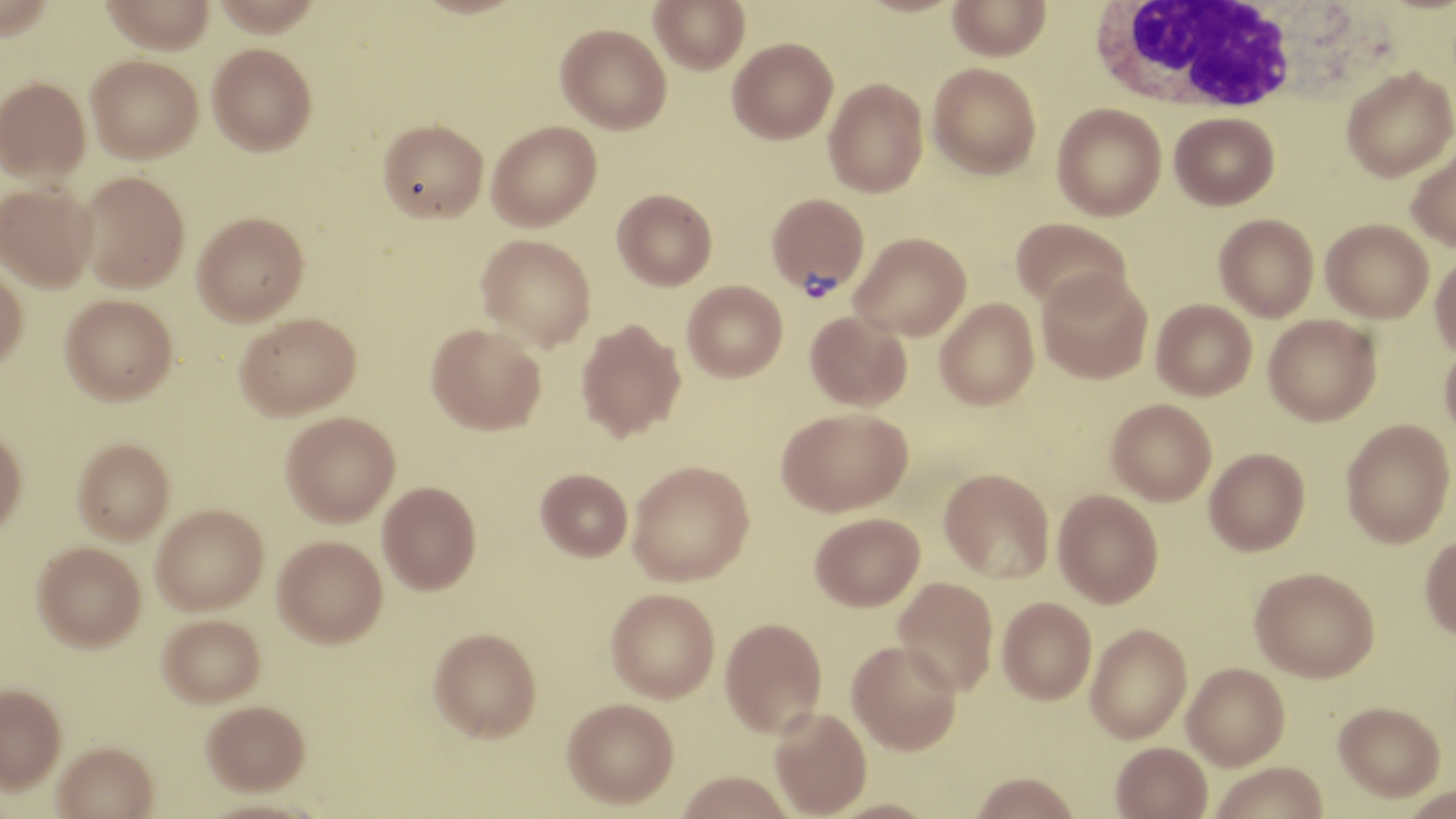

Approximate bounding boxes as named x1/y1/x2/y2 corners in pixels. Plasmodium vivax-infected red blood cell locations: (x1=767, y1=193, x2=869, y2=298). Uninfected red blood cell locations: (x1=99, y1=0, x2=216, y2=54), (x1=649, y1=0, x2=750, y2=74), (x1=947, y1=1, x2=1051, y2=61), (x1=555, y1=23, x2=671, y2=133), (x1=727, y1=37, x2=838, y2=143), (x1=207, y1=43, x2=317, y2=155), (x1=86, y1=55, x2=203, y2=162), (x1=928, y1=62, x2=1041, y2=179), (x1=1341, y1=67, x2=1455, y2=182), (x1=0, y1=76, x2=90, y2=182), (x1=823, y1=78, x2=928, y2=197), (x1=1052, y1=103, x2=1166, y2=220), (x1=1170, y1=112, x2=1279, y2=210), (x1=377, y1=119, x2=488, y2=222), (x1=487, y1=121, x2=602, y2=230), (x1=1406, y1=142, x2=1456, y2=252), (x1=78, y1=171, x2=189, y2=292), (x1=0, y1=182, x2=97, y2=291), (x1=612, y1=189, x2=717, y2=289), (x1=192, y1=212, x2=308, y2=325), (x1=1214, y1=214, x2=1319, y2=321), (x1=1011, y1=217, x2=1131, y2=312), (x1=1321, y1=218, x2=1433, y2=322), (x1=850, y1=232, x2=971, y2=340), (x1=476, y1=234, x2=596, y2=350), (x1=1430, y1=252, x2=1456, y2=358), (x1=0, y1=266, x2=27, y2=370), (x1=1036, y1=268, x2=1153, y2=383), (x1=682, y1=280, x2=788, y2=381), (x1=60, y1=294, x2=177, y2=404), (x1=934, y1=298, x2=1039, y2=409), (x1=1151, y1=299, x2=1257, y2=400), (x1=805, y1=311, x2=911, y2=410), (x1=235, y1=312, x2=361, y2=420), (x1=1263, y1=313, x2=1381, y2=425), (x1=576, y1=320, x2=686, y2=442), (x1=426, y1=323, x2=546, y2=434), (x1=1440, y1=339, x2=1456, y2=444), (x1=1107, y1=399, x2=1217, y2=505), (x1=777, y1=407, x2=912, y2=516), (x1=280, y1=411, x2=400, y2=525), (x1=1341, y1=419, x2=1455, y2=547), (x1=0, y1=428, x2=27, y2=536), (x1=73, y1=438, x2=174, y2=543), (x1=1205, y1=447, x2=1310, y2=555), (x1=628, y1=460, x2=754, y2=586), (x1=939, y1=468, x2=1054, y2=583), (x1=536, y1=469, x2=633, y2=562), (x1=378, y1=482, x2=481, y2=595), (x1=1053, y1=489, x2=1163, y2=607), (x1=151, y1=505, x2=268, y2=615), (x1=811, y1=513, x2=924, y2=613), (x1=1420, y1=532, x2=1456, y2=641), (x1=273, y1=535, x2=387, y2=647), (x1=32, y1=541, x2=146, y2=650), (x1=1250, y1=568, x2=1380, y2=683), (x1=893, y1=578, x2=997, y2=697), (x1=605, y1=590, x2=719, y2=704), (x1=998, y1=599, x2=1097, y2=706), (x1=158, y1=613, x2=265, y2=706), (x1=720, y1=619, x2=827, y2=741), (x1=1086, y1=624, x2=1192, y2=745), (x1=429, y1=628, x2=542, y2=743), (x1=847, y1=643, x2=963, y2=759), (x1=1182, y1=664, x2=1289, y2=772), (x1=0, y1=682, x2=66, y2=791), (x1=202, y1=701, x2=310, y2=796), (x1=562, y1=701, x2=678, y2=812), (x1=1333, y1=704, x2=1445, y2=805), (x1=769, y1=710, x2=871, y2=819), (x1=54, y1=743, x2=159, y2=819), (x1=1111, y1=744, x2=1213, y2=819), (x1=1211, y1=764, x2=1330, y2=819), (x1=676, y1=774, x2=796, y2=819), (x1=970, y1=776, x2=1081, y2=819), (x1=1397, y1=788, x2=1455, y2=819), (x1=826, y1=801, x2=941, y2=819). White blood cell locations: (x1=1086, y1=1, x2=1308, y2=116). Slide-level diagnosis: Plasmodium vivax. Optical microscopy. Image is 1456×819 pixels. May-Grünwald-Giemsa stain. 1000x magnification. One field of a larger specimen. Thin blood smear.